Name the parasite shown.
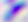
This is Toxoplasma gondii.

modality = photomicrograph
magnification = 400x